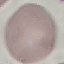
Malaria status: uninfected. Giemsa-stained preparation. Automatically extracted cell patch, resized to 64 × 64 pixels. Acquired by smartphone through the microscope eyepiece. Thin blood film.